Give the position of every Plasmodium parasite.
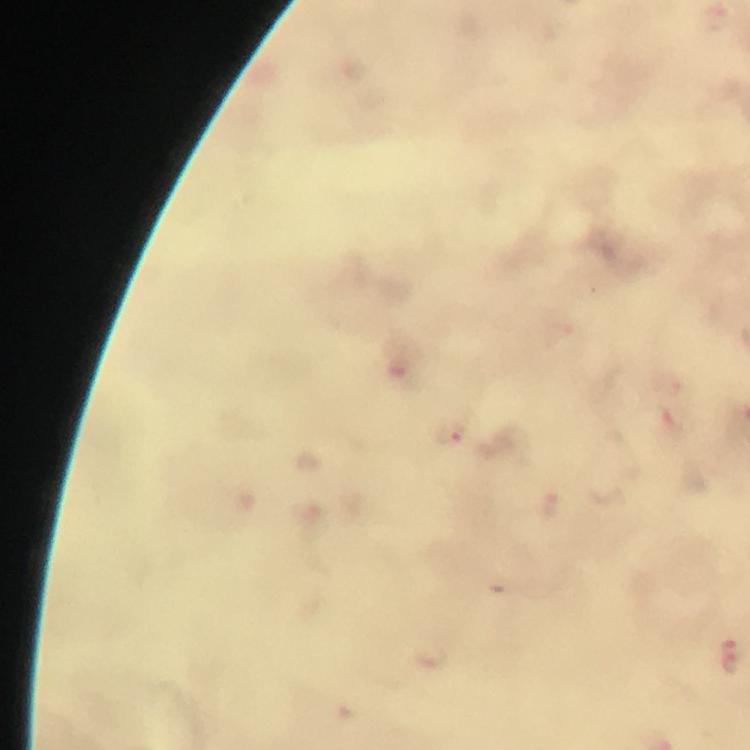

Approximate object centers, in pixels from the top-left corner.
Plasmodium parasites: (x=448, y=432), (x=733, y=656).

image_size: 750×750 pixels
preparation: thick blood film
context: from a malaria diagnostic workup
immersion_oil: used
stain: Giemsa
magnification: 100x
cropped_from: one field of view
capture: smartphone camera through the microscope